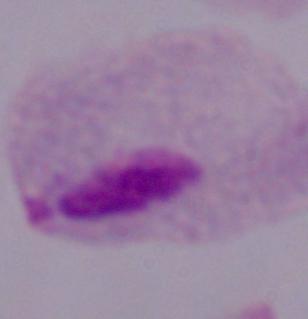 A trichomonad is seen. Captured at 1000x magnification. Micrograph.